State the blood parasite species.
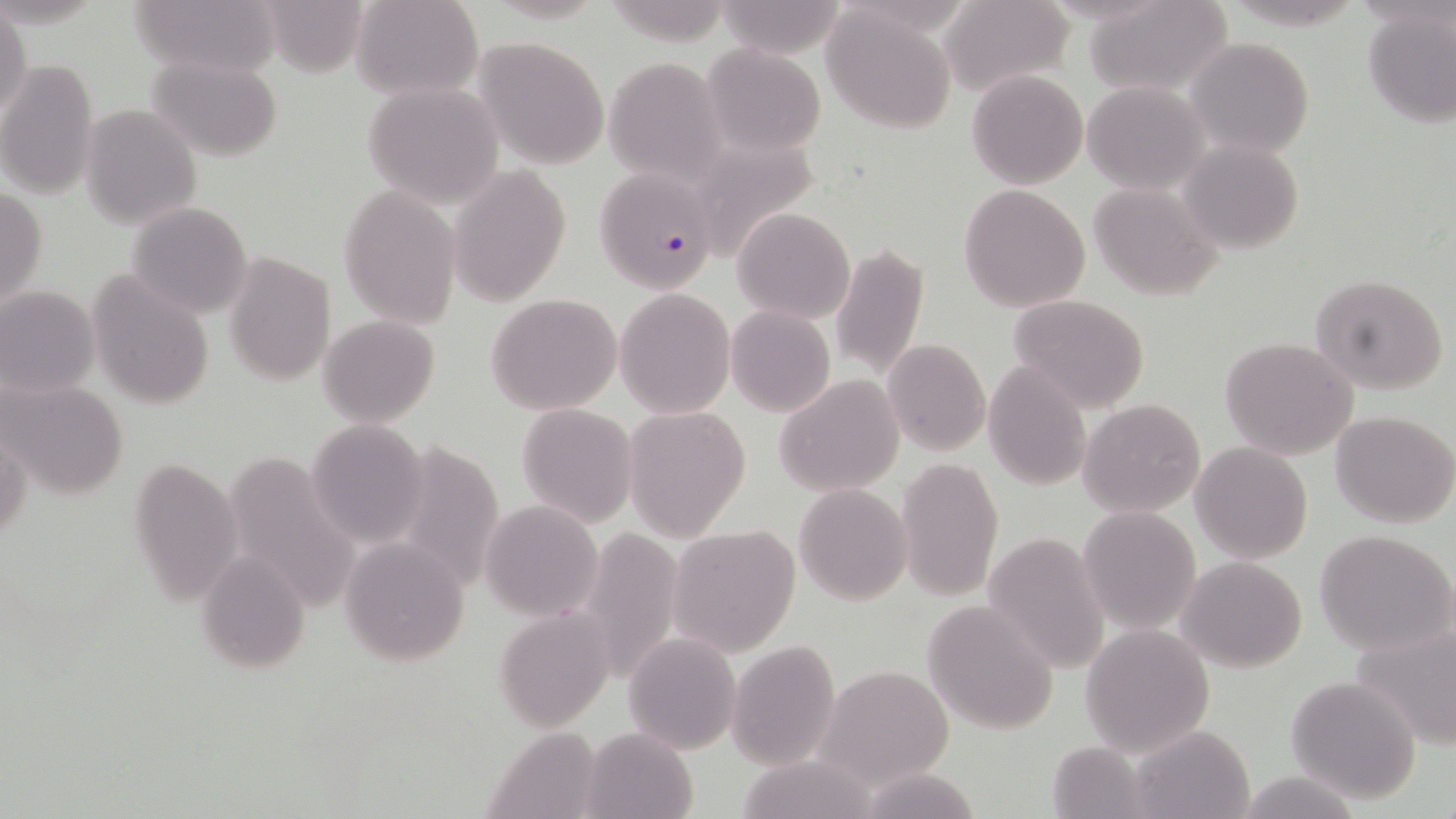

Plasmodium falciparum.

Approximate bounding boxes as [x1, y1, x2, y2] in pixels. Plasmodium falciparum-infected red blood cell locations: [589, 169, 716, 296]. Uninfected red blood cell locations: [131, 0, 281, 77], [351, 0, 483, 102], [713, 0, 851, 60], [939, 0, 1075, 100], [1083, 0, 1234, 100], [254, 1, 370, 75], [823, 5, 957, 133], [1360, 5, 1456, 127], [0, 10, 31, 121], [1183, 35, 1315, 157], [472, 36, 611, 169], [700, 45, 827, 156], [145, 54, 285, 160], [603, 57, 727, 187], [0, 58, 98, 202], [966, 70, 1089, 188], [362, 80, 506, 207], [1083, 81, 1209, 194], [78, 105, 202, 229], [1175, 138, 1308, 257], [692, 143, 833, 268], [449, 164, 570, 308], [1086, 181, 1222, 299], [339, 183, 463, 328], [958, 184, 1090, 313], [1, 185, 47, 313], [126, 202, 254, 318], [731, 206, 856, 323], [831, 243, 927, 383], [223, 250, 336, 388], [1308, 273, 1450, 395], [87, 274, 215, 410], [0, 286, 100, 400], [615, 290, 736, 418], [486, 293, 623, 414], [1008, 294, 1150, 413], [724, 306, 835, 417], [318, 316, 440, 426], [1220, 336, 1359, 461], [881, 337, 990, 455], [981, 361, 1093, 491], [775, 375, 903, 497], [2, 377, 130, 501], [1079, 398, 1205, 519], [516, 403, 638, 527], [623, 405, 750, 542], [1330, 409, 1456, 528], [1, 413, 32, 548], [305, 417, 428, 545], [1190, 441, 1315, 565], [127, 453, 245, 608], [896, 458, 1004, 601], [794, 483, 911, 605], [479, 501, 601, 620], [1076, 505, 1201, 633], [667, 523, 802, 657], [573, 525, 684, 687], [1313, 529, 1455, 656], [980, 532, 1109, 672], [343, 536, 472, 664], [197, 544, 315, 671], [1177, 555, 1308, 673], [922, 598, 1060, 735], [494, 608, 616, 732], [1349, 619, 1456, 747], [1080, 623, 1215, 756], [623, 633, 742, 754], [727, 640, 842, 772], [818, 664, 955, 788], [1284, 674, 1423, 804], [1127, 725, 1256, 818], [580, 727, 697, 818], [482, 728, 606, 819], [1046, 740, 1150, 818], [733, 755, 886, 819], [853, 765, 985, 819], [1237, 771, 1361, 818]. Single field of view. 1000x magnification. Thin blood smear. May-Grünwald-Giemsa stain. Light microscopy. Image is 1456×819 pixels.